Identify the parasite.
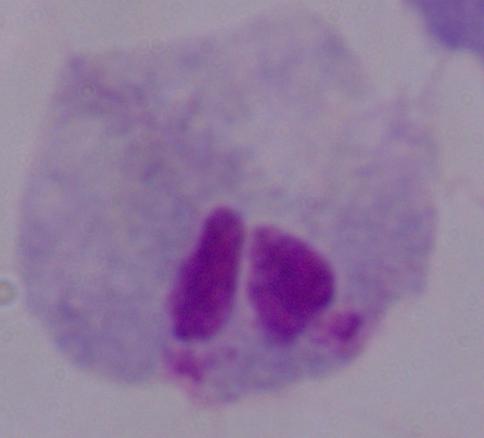

A trichomonad.

Summary:
  - Modality: micrograph
  - Magnification: 1000x